Locate and identify every blood parasite.
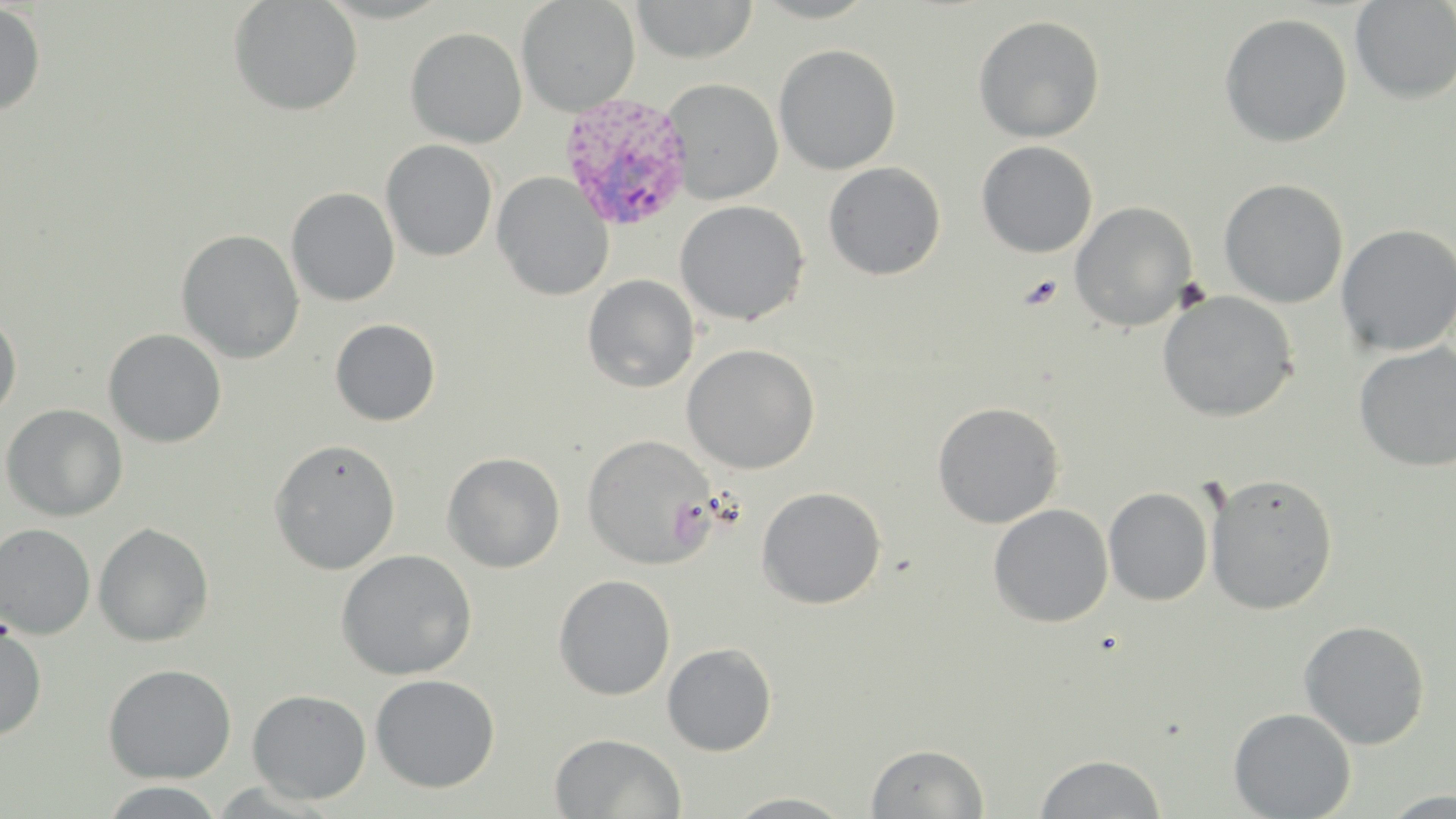
Approximate bounding boxes as (x1, y1, x2, y2) in pixels.
Plasmodium vivax-infected red blood cells: (558, 92, 696, 232).
No Plasmodium falciparum, Plasmodium ovale, Plasmodium malariae, Babesia divergens, or Trypanosoma brucei observed.

slide-level diagnosis = Plasmodium vivax
uninfected red blood cell locations = approximate bounding boxes as (x1, y1, x2, y2) in pixels: (228, 0, 363, 116), (516, 0, 640, 115), (1350, 0, 1456, 104), (630, 1, 758, 63), (0, 3, 46, 117), (1219, 12, 1353, 148), (972, 14, 1105, 143), (405, 26, 527, 148), (774, 44, 901, 175), (661, 78, 783, 204), (381, 139, 498, 262), (976, 140, 1098, 258), (823, 162, 946, 281), (492, 172, 614, 300), (1219, 178, 1349, 308), (286, 187, 400, 306), (674, 200, 810, 325), (1070, 201, 1198, 331), (1335, 223, 1456, 357), (175, 228, 304, 363), (582, 274, 700, 392), (1157, 290, 1299, 422), (0, 311, 22, 422), (330, 318, 441, 426), (103, 328, 227, 448), (1353, 342, 1456, 472), (681, 343, 820, 474), (932, 401, 1065, 528), (1, 404, 128, 521), (582, 434, 717, 570), (268, 438, 401, 575), (442, 452, 565, 572), (1204, 471, 1339, 615), (756, 486, 887, 609), (1103, 487, 1214, 606), (989, 503, 1113, 627), (93, 522, 214, 647), (0, 523, 96, 639), (336, 549, 477, 680), (356, 551, 486, 795), (553, 574, 675, 700), (1298, 619, 1431, 750), (0, 622, 47, 741), (662, 642, 777, 756), (102, 663, 237, 783), (369, 674, 500, 793), (247, 688, 372, 804), (1228, 707, 1357, 819), (550, 733, 686, 818), (866, 743, 989, 818), (1033, 753, 1168, 818), (96, 782, 229, 818), (1381, 790, 1456, 817), (722, 792, 859, 818)
image size = 1456×819 pixels
modality = light microscopy
stain = May-Grünwald-Giemsa
field of view = one of a larger specimen
magnification = 1000x
preparation = thin blood smear